Comment on the morphology of the erythrocytes.
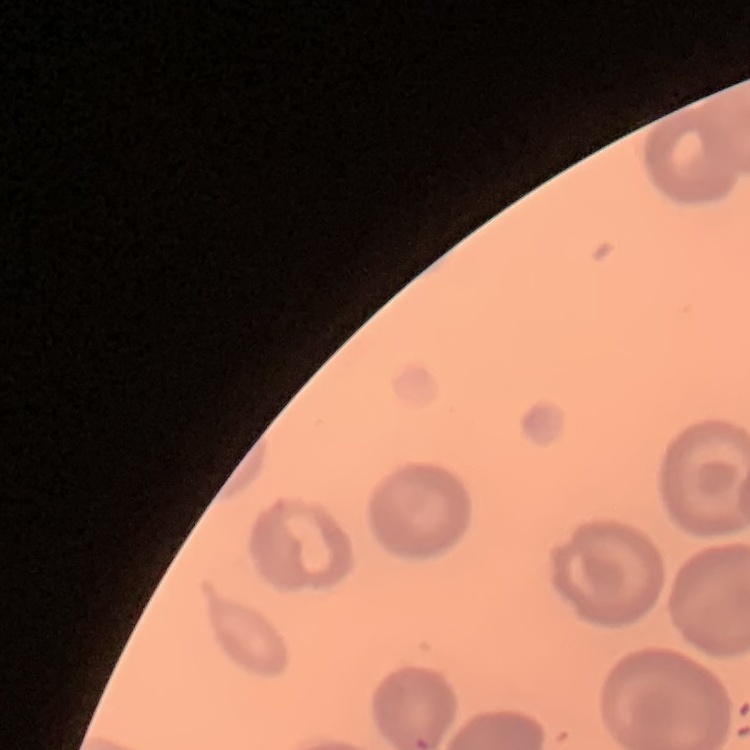

They show no rouleaux formation.

preparation = thin blood smear
image type = one tile cut from a larger photomicrograph
stain = Field's or Giemsa